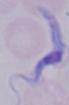
identification = trypanosome
modality = photomicrograph
magnification = 1000x